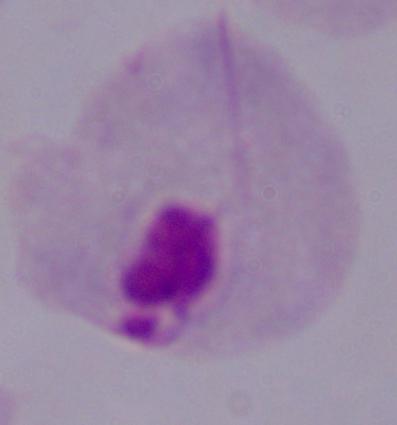 1000x magnification. A trichomonad is seen. Micrograph.